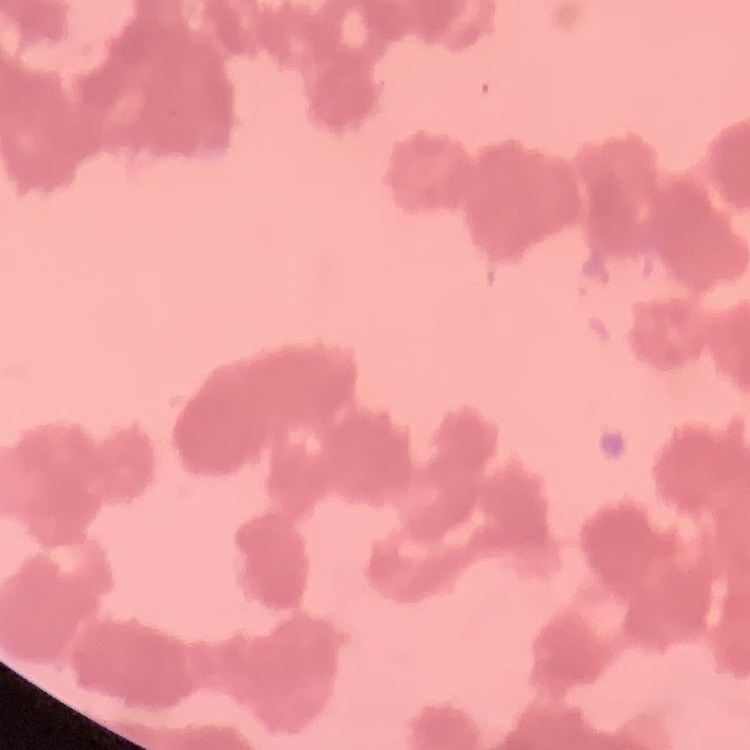
The erythrocytes show rouleaux formation. One tile cut from a larger photomicrograph. Thin peripheral smear. Field's or Giemsa stain.